Locate and identify every blood parasite.
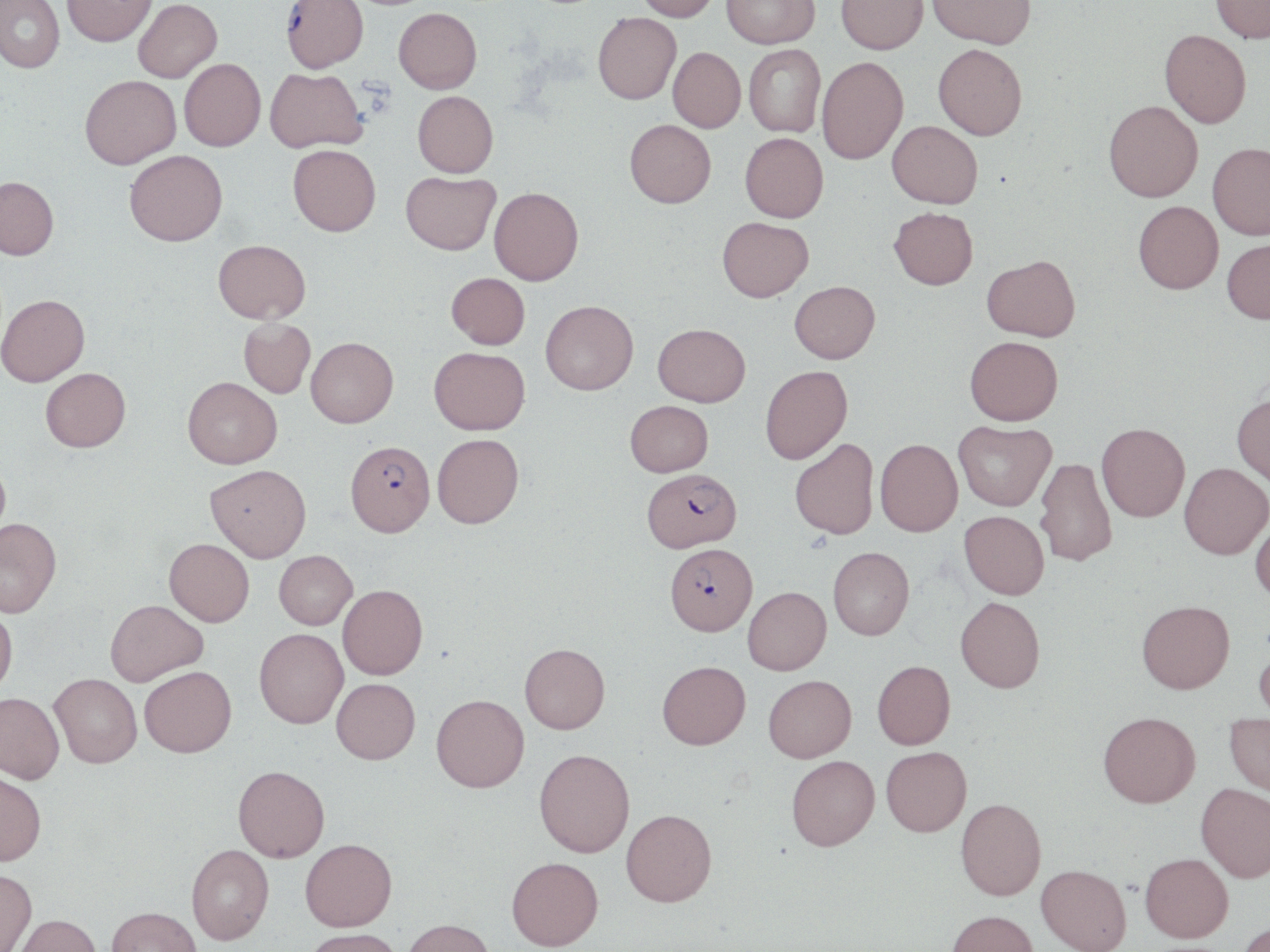

Approximate bounding boxes as (x1, y1, x2, y2) in pixels.
Plasmodium falciparum-infected red blood cells: (281, 0, 369, 75), (345, 440, 435, 536), (642, 468, 742, 553), (664, 542, 757, 636).
No Plasmodium ovale, Plasmodium malariae, Plasmodium vivax, Babesia divergens, or Trypanosoma brucei observed.

Summary:
  - Uninfected red blood cell locations: (0, 0, 64, 74), (62, 0, 156, 49), (133, 0, 222, 84), (636, 0, 720, 24), (721, 0, 819, 51), (836, 0, 928, 58), (927, 0, 1035, 52), (1210, 0, 1270, 45), (394, 9, 482, 95), (593, 15, 681, 107), (1159, 32, 1251, 130), (744, 46, 825, 138), (933, 47, 1027, 143), (668, 50, 745, 134), (180, 59, 265, 152), (817, 60, 908, 167), (265, 68, 367, 154), (80, 76, 181, 171), (413, 92, 498, 179), (1103, 102, 1203, 203), (625, 121, 715, 210), (887, 122, 982, 210), (740, 133, 828, 224), (1208, 142, 1270, 240), (287, 144, 381, 236), (125, 150, 228, 247), (402, 170, 500, 256), (0, 176, 58, 260), (489, 187, 583, 285), (1134, 200, 1223, 295), (889, 207, 978, 290), (717, 216, 814, 302), (1222, 238, 1270, 325), (213, 239, 311, 323), (982, 254, 1080, 341), (446, 273, 530, 349), (790, 281, 880, 364), (0, 294, 90, 386), (540, 300, 639, 396), (239, 318, 315, 398), (653, 323, 751, 406), (964, 335, 1062, 426), (305, 336, 399, 428), (429, 347, 530, 434), (760, 365, 852, 464), (40, 367, 131, 452), (182, 377, 282, 468), (1232, 394, 1270, 487), (625, 400, 713, 477), (953, 420, 1056, 510), (1097, 422, 1190, 521), (432, 434, 524, 528), (790, 438, 879, 539), (875, 438, 963, 536), (0, 458, 11, 546), (1035, 458, 1116, 567), (1179, 462, 1270, 559), (205, 464, 311, 561), (959, 510, 1049, 599), (1250, 516, 1270, 605), (0, 517, 62, 617), (164, 538, 254, 626), (828, 547, 914, 640), (274, 550, 357, 629), (337, 584, 427, 680), (743, 587, 831, 675), (955, 596, 1045, 692), (105, 599, 207, 686), (1137, 600, 1234, 693), (0, 605, 17, 696), (254, 628, 348, 728), (519, 643, 610, 733), (1254, 644, 1270, 728), (657, 660, 750, 749), (872, 660, 955, 749), (139, 666, 236, 756), (50, 673, 142, 767), (763, 675, 856, 762), (331, 678, 420, 763), (0, 692, 64, 784), (431, 694, 529, 792), (1098, 711, 1200, 807), (1225, 716, 1270, 798), (881, 746, 972, 836), (534, 748, 635, 857), (787, 755, 880, 850), (233, 765, 330, 861), (0, 770, 46, 865), (1195, 782, 1270, 881), (956, 798, 1046, 900), (621, 808, 717, 906), (300, 838, 397, 931), (186, 843, 274, 944), (1140, 852, 1233, 942), (506, 856, 604, 950), (1036, 864, 1131, 952), (0, 868, 37, 952), (106, 906, 201, 952), (947, 909, 1039, 952), (13, 913, 101, 952), (403, 918, 495, 952), (1238, 919, 1270, 952), (303, 928, 405, 952)
  - Slide-level diagnosis: Plasmodium falciparum
  - Modality: optical microscopy
  - Preparation: thin blood film
  - Stain: May-Grünwald-Giemsa
  - Field of view: one of a larger specimen
  - Magnification: 1000x
  - Image size: 1270×952 pixels